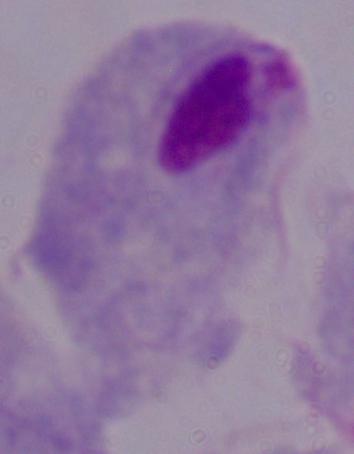
Summary:
  - Modality: micrograph
  - Magnification: 1000x
  - Identification: trichomonad